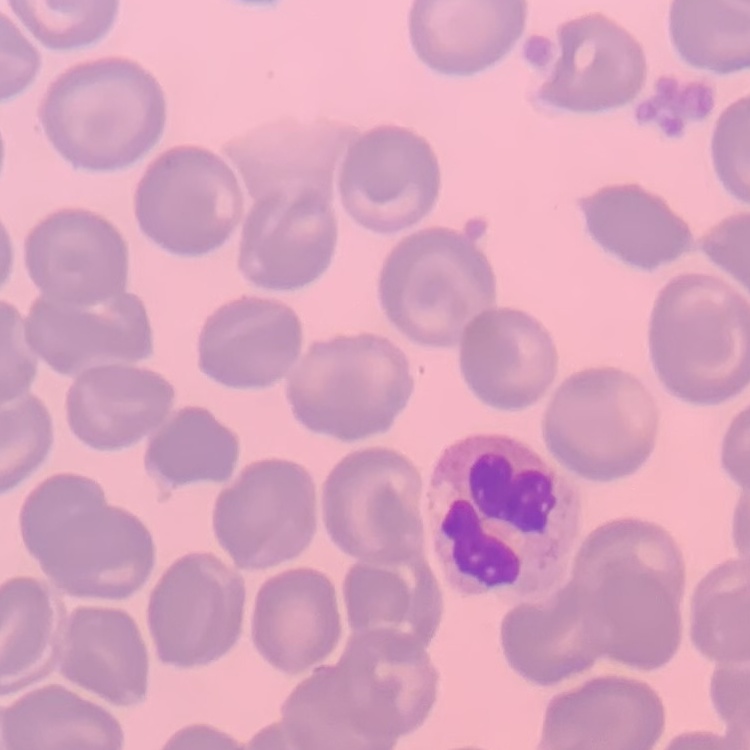

The red blood cells exhibit no rouleaux formation. Stained with either Field's or Giemsa. Thin peripheral smear. One tile cut from a larger photomicrograph.